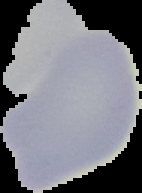 From a thin blood film. Image is 142×193 pixels. Malaria status: uninfected. Cell region segmented out of the field of view; the surrounding area is masked to black.